Locate every Plasmodium malariae-infected red blood cell.
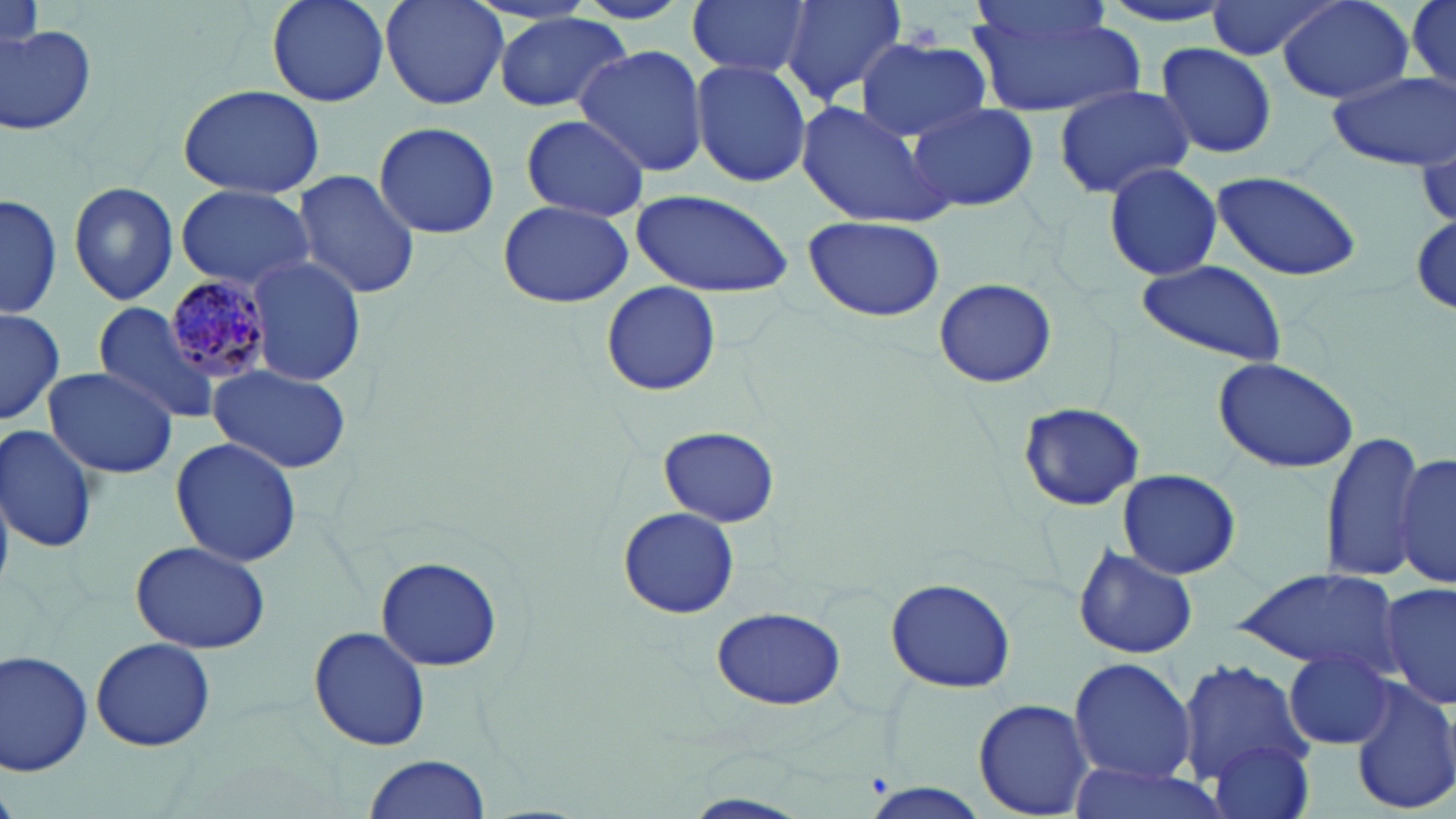
Approximate bounding boxes as (x1,y1)-(x2,y2) corner pairs in pixels.
Plasmodium malariae-infected red blood cells: (163,274)-(277,382).

Summary:
  - Uninfected red blood cell locations: (263,0)-(390,108), (379,0)-(509,111), (687,0)-(813,79), (776,0)-(908,106), (1089,0)-(1243,33), (1278,0)-(1414,105), (969,1)-(1118,53), (1203,1)-(1345,61), (966,5)-(1141,117), (489,15)-(632,113), (0,22)-(98,137), (855,38)-(991,140), (1154,42)-(1278,160), (575,44)-(708,176), (691,61)-(811,187), (1326,70)-(1456,171), (1050,82)-(1195,199), (177,85)-(328,199), (797,99)-(955,230), (906,100)-(1038,213), (519,114)-(651,221), (372,121)-(500,240), (1102,162)-(1224,280), (292,170)-(421,300), (1209,172)-(1363,280), (67,180)-(178,305), (175,185)-(315,293), (630,189)-(795,300), (1,193)-(63,318), (498,200)-(633,308), (1407,212)-(1456,323), (803,215)-(947,324), (244,255)-(369,385), (1133,259)-(1288,370), (934,279)-(1057,388), (599,280)-(721,396), (92,302)-(224,427), (0,306)-(66,422), (1210,355)-(1360,473), (208,363)-(353,473), (43,365)-(179,480), (1018,403)-(1144,510), (0,425)-(101,554), (658,426)-(779,528), (1320,432)-(1425,584), (170,437)-(302,568), (1394,449)-(1456,590), (1116,469)-(1242,579), (617,508)-(739,618), (130,540)-(270,653), (1070,544)-(1199,661), (376,556)-(502,673), (1233,567)-(1403,673), (883,577)-(1018,695), (1379,580)-(1456,713), (711,606)-(846,711), (308,626)-(432,752), (90,636)-(216,752), (1,650)-(96,777), (1282,650)-(1394,750), (1067,656)-(1197,785), (1177,657)-(1312,789), (1350,678)-(1456,818), (973,698)-(1095,816), (1208,740)-(1318,819), (363,754)-(491,819), (1063,760)-(1234,819), (863,784)-(988,818), (677,794)-(813,819)
  - Slide-level diagnosis: Plasmodium malariae
  - Preparation: thin blood smear
  - Stain: May-Grünwald-Giemsa
  - Image size: 1456×819 pixels
  - Modality: light microscopy
  - Magnification: 1000x
  - Field of view: single